State which cell type is depicted.
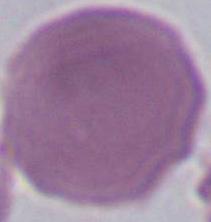
This is an erythrocyte.

magnification: 1000x
modality: photomicrograph